Locate platelets.
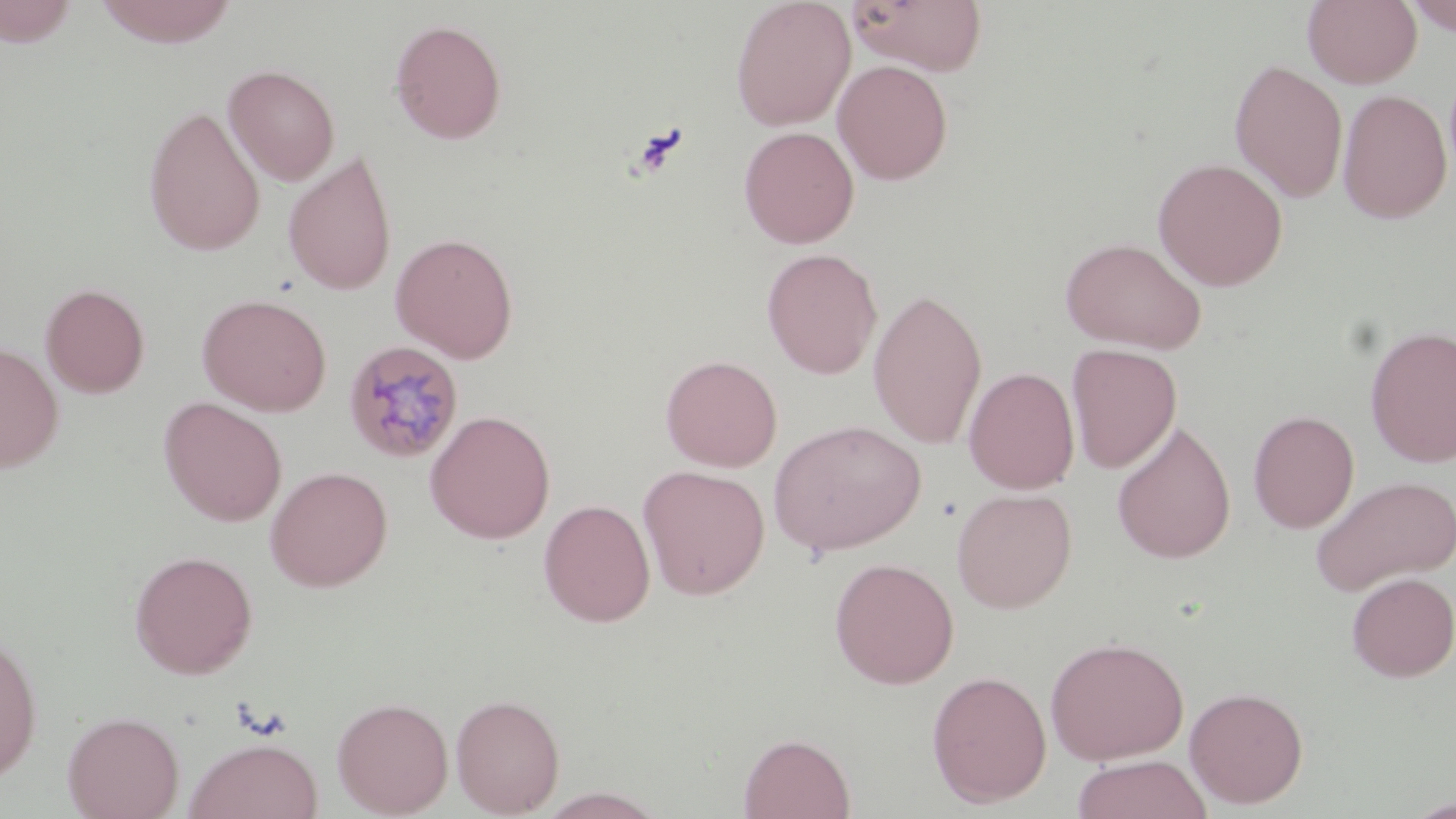
Approximate bounding boxes as named x1/y1/x2/y2 corners in pixels.
Platelets: (x1=629, y1=122, x2=689, y2=178).

Uninfected red blood cell locations: (x1=93, y1=0, x2=240, y2=47), (x1=730, y1=0, x2=856, y2=131), (x1=846, y1=0, x2=988, y2=76), (x1=1302, y1=0, x2=1422, y2=88), (x1=1401, y1=0, x2=1456, y2=36), (x1=0, y1=1, x2=82, y2=47), (x1=389, y1=18, x2=507, y2=144), (x1=832, y1=59, x2=953, y2=185), (x1=1228, y1=59, x2=1348, y2=204), (x1=223, y1=64, x2=340, y2=186), (x1=1337, y1=89, x2=1452, y2=224), (x1=143, y1=105, x2=265, y2=257), (x1=738, y1=125, x2=859, y2=249), (x1=282, y1=152, x2=398, y2=296), (x1=1152, y1=156, x2=1288, y2=291), (x1=390, y1=232, x2=519, y2=363), (x1=1059, y1=236, x2=1208, y2=354), (x1=761, y1=248, x2=882, y2=379), (x1=40, y1=282, x2=150, y2=399), (x1=868, y1=287, x2=988, y2=450), (x1=197, y1=293, x2=332, y2=416), (x1=1365, y1=324, x2=1456, y2=468), (x1=0, y1=341, x2=64, y2=473), (x1=1066, y1=343, x2=1182, y2=474), (x1=660, y1=354, x2=783, y2=472), (x1=964, y1=367, x2=1080, y2=494), (x1=158, y1=397, x2=287, y2=526), (x1=1248, y1=409, x2=1359, y2=533), (x1=425, y1=410, x2=556, y2=544), (x1=768, y1=420, x2=926, y2=557), (x1=1111, y1=421, x2=1236, y2=564), (x1=638, y1=464, x2=771, y2=600), (x1=264, y1=465, x2=393, y2=591), (x1=1310, y1=474, x2=1456, y2=597), (x1=951, y1=487, x2=1077, y2=613), (x1=538, y1=499, x2=655, y2=627), (x1=129, y1=550, x2=258, y2=679), (x1=829, y1=557, x2=959, y2=689), (x1=1346, y1=571, x2=1456, y2=682), (x1=0, y1=631, x2=42, y2=782), (x1=1045, y1=635, x2=1189, y2=765), (x1=926, y1=669, x2=1052, y2=807), (x1=1184, y1=686, x2=1309, y2=809), (x1=450, y1=693, x2=565, y2=817), (x1=332, y1=697, x2=454, y2=817), (x1=62, y1=710, x2=185, y2=819), (x1=737, y1=732, x2=856, y2=818), (x1=182, y1=737, x2=324, y2=819), (x1=1070, y1=754, x2=1211, y2=819), (x1=536, y1=788, x2=668, y2=819). Plasmodium malariae-infected red blood cell locations: (x1=343, y1=340, x2=466, y2=464). Slide-level diagnosis: Plasmodium malariae. Light microscopy. May-Grünwald-Giemsa-stained preparation. One field of a larger specimen. 1000x magnification. Thin blood film. Image is 1456×819 pixels.